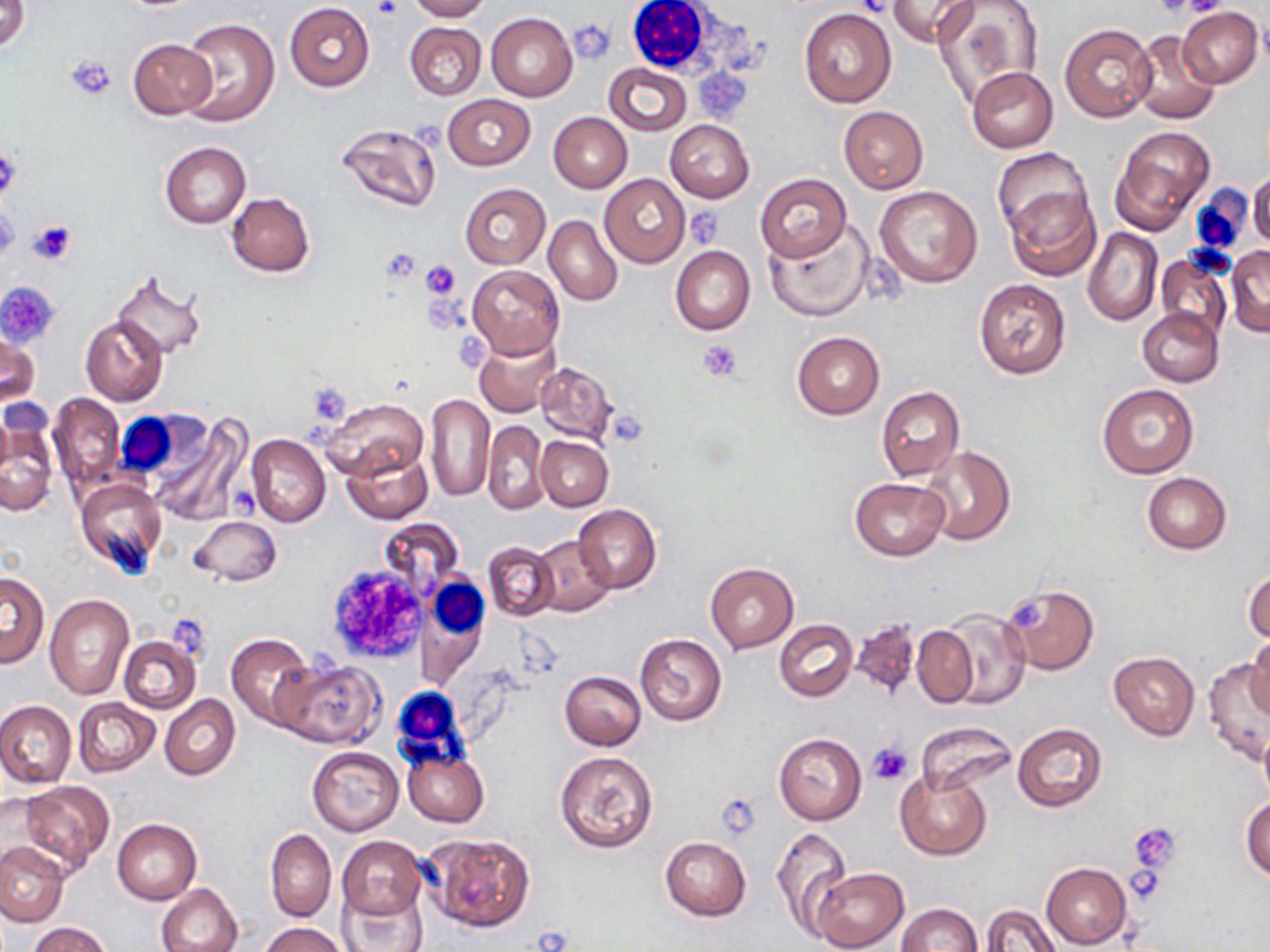
Summary:
  - Coordinate format: approximate bounding boxes as (x1, y1, x2, y2) in pixels
  - Uninfected red blood cell locations: (1, 0, 30, 53), (406, 0, 490, 22), (932, 0, 1043, 107), (889, 1, 980, 47), (284, 3, 374, 92), (1178, 7, 1262, 86), (798, 9, 897, 109), (486, 12, 578, 101), (179, 16, 280, 127), (404, 21, 487, 101), (1059, 23, 1157, 123), (1129, 30, 1220, 125), (128, 37, 217, 120), (603, 64, 691, 136), (968, 67, 1059, 152), (443, 94, 535, 169), (838, 106, 928, 193), (549, 112, 632, 193), (665, 120, 755, 203), (334, 121, 442, 214), (1111, 127, 1214, 231), (160, 142, 251, 229), (993, 147, 1091, 237), (1248, 171, 1270, 248), (600, 173, 689, 267), (755, 173, 851, 261), (459, 183, 551, 269), (873, 185, 983, 287), (1005, 185, 1100, 281), (226, 192, 315, 277), (543, 214, 622, 306), (764, 222, 874, 322), (1083, 227, 1163, 326), (670, 244, 756, 336), (1225, 244, 1270, 338), (1153, 252, 1233, 340), (466, 264, 564, 359), (112, 274, 206, 362), (972, 277, 1071, 380), (1136, 307, 1223, 386), (79, 315, 169, 407), (1, 327, 39, 413), (791, 332, 884, 420), (474, 334, 560, 418), (534, 359, 617, 443), (1097, 384, 1199, 478), (876, 386, 965, 482), (48, 393, 126, 493), (425, 394, 494, 500), (319, 398, 427, 482), (1, 409, 61, 514), (149, 415, 249, 524), (482, 420, 550, 515), (246, 433, 330, 528), (536, 436, 613, 510), (918, 445, 1016, 546), (341, 446, 432, 525), (1143, 472, 1231, 553), (75, 477, 164, 574), (849, 477, 950, 561), (573, 504, 661, 593), (189, 516, 282, 586), (531, 534, 614, 615), (483, 542, 558, 621), (705, 563, 799, 653), (1244, 565, 1270, 645), (1, 572, 48, 667), (999, 584, 1098, 675), (45, 593, 133, 698), (937, 610, 1031, 709), (850, 616, 920, 698), (774, 619, 858, 702), (911, 625, 978, 708), (634, 632, 727, 725), (226, 633, 314, 726), (119, 636, 201, 714), (1247, 636, 1270, 718), (1108, 652, 1200, 739), (273, 657, 383, 748), (1203, 659, 1269, 765), (559, 671, 647, 751), (160, 694, 240, 780), (73, 697, 160, 777), (0, 700, 76, 788), (913, 722, 1017, 794), (1012, 722, 1107, 812), (1258, 728, 1270, 808), (773, 733, 867, 824), (307, 745, 404, 834), (554, 749, 659, 854), (403, 751, 488, 827), (894, 768, 991, 859), (20, 781, 115, 870), (0, 793, 64, 880), (1241, 793, 1270, 881), (111, 818, 202, 904), (770, 826, 851, 933), (265, 828, 336, 922), (423, 832, 535, 932), (337, 836, 426, 919), (659, 836, 751, 921), (0, 840, 68, 927), (1041, 861, 1131, 949), (809, 866, 908, 952), (156, 884, 243, 952), (339, 886, 430, 952), (895, 903, 983, 952), (980, 903, 1059, 952), (26, 922, 114, 952), (261, 922, 347, 952)
  - White blood cell locations: (624, 0, 719, 76), (1187, 184, 1253, 256), (119, 410, 212, 480), (419, 573, 489, 666), (387, 681, 476, 769)
  - Platelet locations: (375, 0, 401, 21), (855, 0, 894, 19), (1154, 0, 1211, 17), (1178, 0, 1229, 18), (571, 20, 613, 63), (66, 54, 118, 100), (412, 118, 447, 151), (0, 145, 21, 201), (0, 197, 20, 264), (684, 209, 724, 247), (28, 220, 76, 265), (380, 247, 421, 282), (420, 259, 461, 299), (3, 279, 59, 343), (701, 340, 742, 381), (326, 563, 429, 665), (1010, 599, 1047, 628), (867, 742, 912, 785), (716, 794, 762, 841), (1129, 821, 1181, 879), (1127, 869, 1166, 901)
  - Slide-level diagnosis: no evidence of blood parasites
  - Preparation: thin blood film
  - Image size: 1270×952 pixels
  - Stain: May-Grünwald-Giemsa
  - Modality: light microscopy
  - Field of view: single
  - Magnification: 1000x